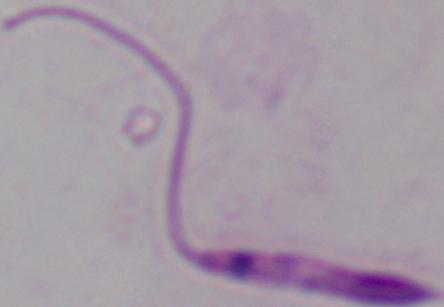
Summary:
  - Modality: photomicrograph
  - Identification: Leishmania
  - Magnification: 1000x